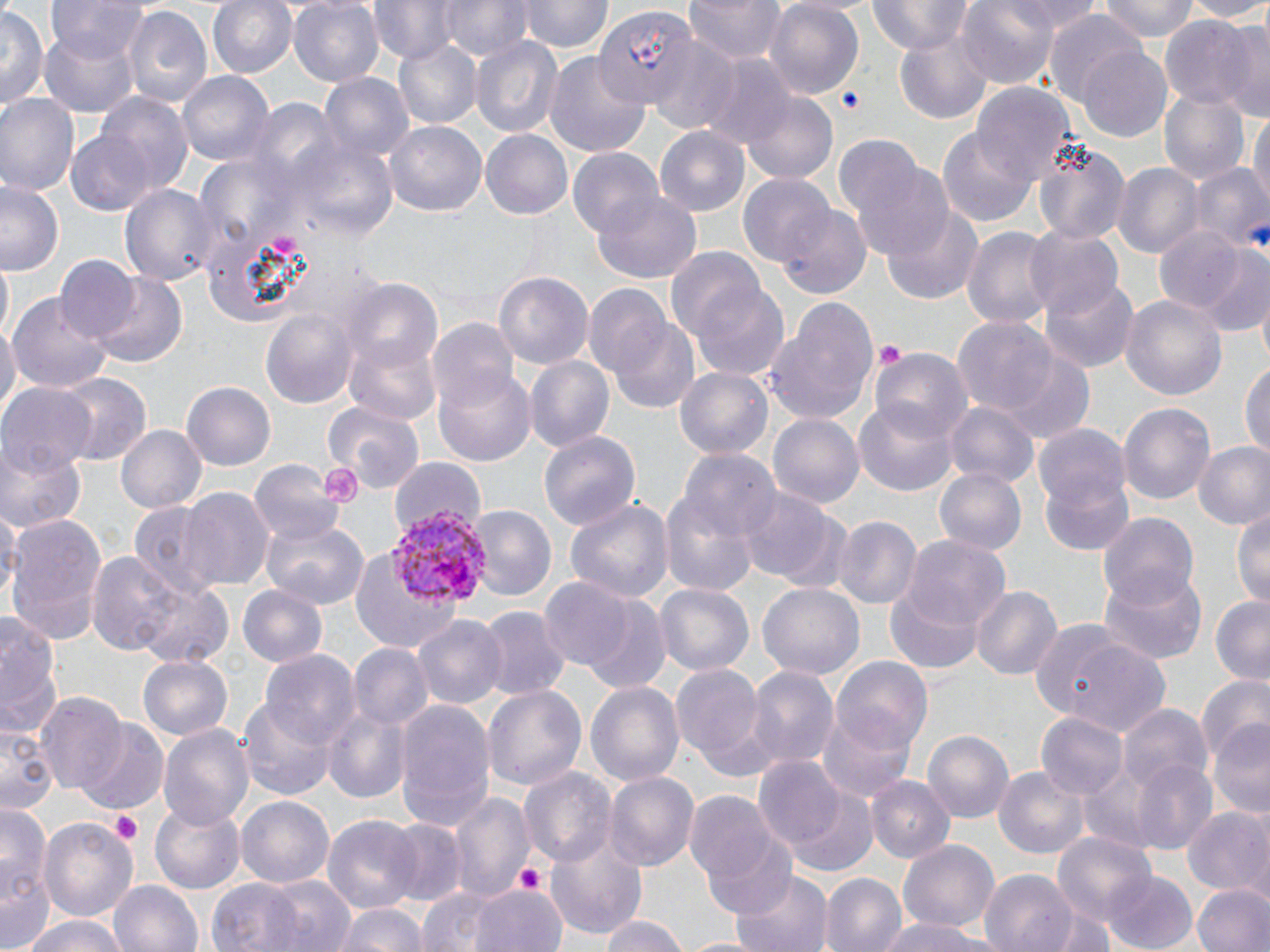

Summary:
  - Coordinate format: approximate bounding boxes as (x1, y1, x2, y2) in pixels
  - Plasmodium vivax-infected red blood cell locations: (384, 505, 489, 610)
  - Platelet locations: (876, 339, 904, 370), (108, 811, 142, 845), (511, 860, 548, 896)
  - Uninfected red blood cell locations: (46, 0, 150, 64), (205, 0, 299, 80), (289, 0, 384, 88), (438, 0, 532, 61), (521, 0, 612, 56), (684, 0, 786, 63), (766, 0, 865, 97), (868, 0, 972, 54), (957, 0, 1063, 88), (1097, 0, 1201, 40), (1181, 0, 1270, 22), (370, 4, 463, 68), (122, 5, 212, 111), (0, 6, 45, 113), (594, 9, 694, 107), (1044, 10, 1144, 107), (1161, 16, 1260, 110), (1223, 21, 1269, 122), (893, 23, 995, 128), (39, 25, 141, 119), (470, 34, 562, 140), (646, 36, 741, 134), (391, 37, 481, 131), (1078, 48, 1172, 141), (546, 49, 652, 159), (699, 56, 796, 149), (177, 71, 273, 169), (321, 74, 413, 166), (973, 83, 1078, 190), (1160, 89, 1251, 183), (0, 92, 79, 198), (742, 92, 841, 185), (95, 93, 195, 196), (1250, 109, 1269, 219), (386, 122, 486, 219), (656, 127, 751, 217), (938, 127, 1037, 228), (66, 130, 155, 216), (287, 131, 401, 247), (481, 132, 571, 218), (834, 137, 928, 232), (1032, 139, 1132, 245), (568, 148, 664, 238), (854, 161, 955, 262), (1114, 163, 1203, 260), (1190, 164, 1270, 253), (738, 173, 836, 265), (1, 181, 64, 273), (121, 182, 219, 288), (593, 192, 701, 281), (772, 202, 873, 303), (883, 207, 983, 303), (1153, 224, 1248, 316), (962, 225, 1056, 331), (1026, 226, 1124, 321), (1199, 246, 1270, 338), (668, 249, 768, 347), (54, 256, 142, 343), (1, 258, 15, 340), (493, 270, 593, 369), (87, 275, 186, 367), (687, 275, 789, 383), (1041, 277, 1137, 371), (343, 280, 442, 377), (584, 282, 693, 406), (8, 290, 112, 397), (1120, 292, 1227, 403), (765, 299, 880, 426), (261, 306, 358, 409), (953, 315, 1058, 414), (428, 319, 518, 412), (0, 320, 19, 421), (344, 339, 441, 428), (871, 347, 973, 439), (1000, 350, 1094, 445), (523, 355, 613, 453), (1241, 359, 1269, 462), (674, 365, 774, 460), (435, 369, 534, 466), (57, 373, 149, 464), (182, 382, 276, 471), (1, 385, 95, 470), (1118, 400, 1216, 510), (323, 401, 428, 495), (944, 402, 1037, 488), (854, 404, 957, 495), (768, 411, 864, 507), (116, 424, 205, 515), (1035, 428, 1135, 552), (541, 429, 642, 530), (0, 440, 84, 534), (1193, 441, 1270, 532), (679, 449, 779, 544), (248, 458, 343, 548), (388, 460, 487, 541), (933, 467, 1027, 558), (182, 488, 274, 592), (740, 489, 834, 584), (564, 495, 674, 606), (661, 495, 758, 596), (127, 501, 230, 595), (1232, 504, 1269, 607), (1, 506, 19, 613), (466, 506, 557, 601), (1096, 510, 1199, 609), (5, 514, 109, 646), (259, 514, 371, 610), (834, 515, 921, 609), (904, 535, 1012, 636), (349, 544, 457, 651), (83, 547, 217, 664), (1096, 565, 1207, 669), (131, 575, 236, 669), (538, 580, 634, 669), (759, 583, 862, 681), (656, 584, 752, 675), (237, 585, 328, 668), (972, 585, 1062, 681), (885, 587, 984, 673), (1210, 596, 1270, 684), (583, 598, 670, 695), (478, 607, 570, 700), (0, 608, 64, 742), (414, 615, 507, 709), (1039, 627, 1171, 738), (348, 644, 431, 732), (263, 647, 358, 747), (137, 651, 233, 739), (832, 657, 933, 756), (673, 659, 768, 768), (747, 666, 838, 771), (1195, 676, 1270, 769), (586, 680, 686, 787), (482, 683, 587, 793), (39, 693, 130, 795), (240, 698, 335, 798), (393, 699, 496, 833), (1119, 703, 1213, 798), (325, 704, 411, 805), (818, 709, 916, 801), (1038, 712, 1127, 801), (1206, 719, 1270, 821), (76, 721, 168, 813), (2, 724, 56, 813), (159, 725, 252, 827), (925, 731, 1013, 821), (753, 757, 847, 854), (1130, 758, 1220, 853), (994, 765, 1088, 859), (518, 767, 617, 869), (606, 771, 698, 871), (867, 775, 955, 864), (787, 787, 879, 876), (686, 790, 784, 889), (447, 793, 534, 901), (236, 795, 334, 888), (0, 800, 52, 943), (151, 800, 245, 892), (1182, 805, 1270, 898), (325, 815, 420, 912), (39, 817, 138, 925), (384, 817, 465, 905), (544, 828, 648, 941), (704, 834, 803, 921), (1053, 834, 1157, 929), (896, 839, 999, 932), (733, 869, 832, 952), (979, 870, 1079, 952), (1103, 871, 1197, 952), (820, 873, 906, 952), (262, 875, 356, 952), (208, 876, 305, 950), (110, 878, 201, 952), (1192, 883, 1270, 952), (469, 885, 568, 952), (418, 887, 496, 952), (334, 902, 430, 952), (1042, 903, 1119, 952), (22, 913, 132, 952), (597, 915, 694, 952), (881, 917, 995, 952)
  - Slide-level diagnosis: Plasmodium vivax
  - Magnification: 1000x
  - Preparation: thin blood smear
  - Image size: 1270×952 pixels
  - Field of view: single
  - Modality: light microscopy
  - Stain: May-Grünwald-Giemsa